Outline each uninfected red blood cell.
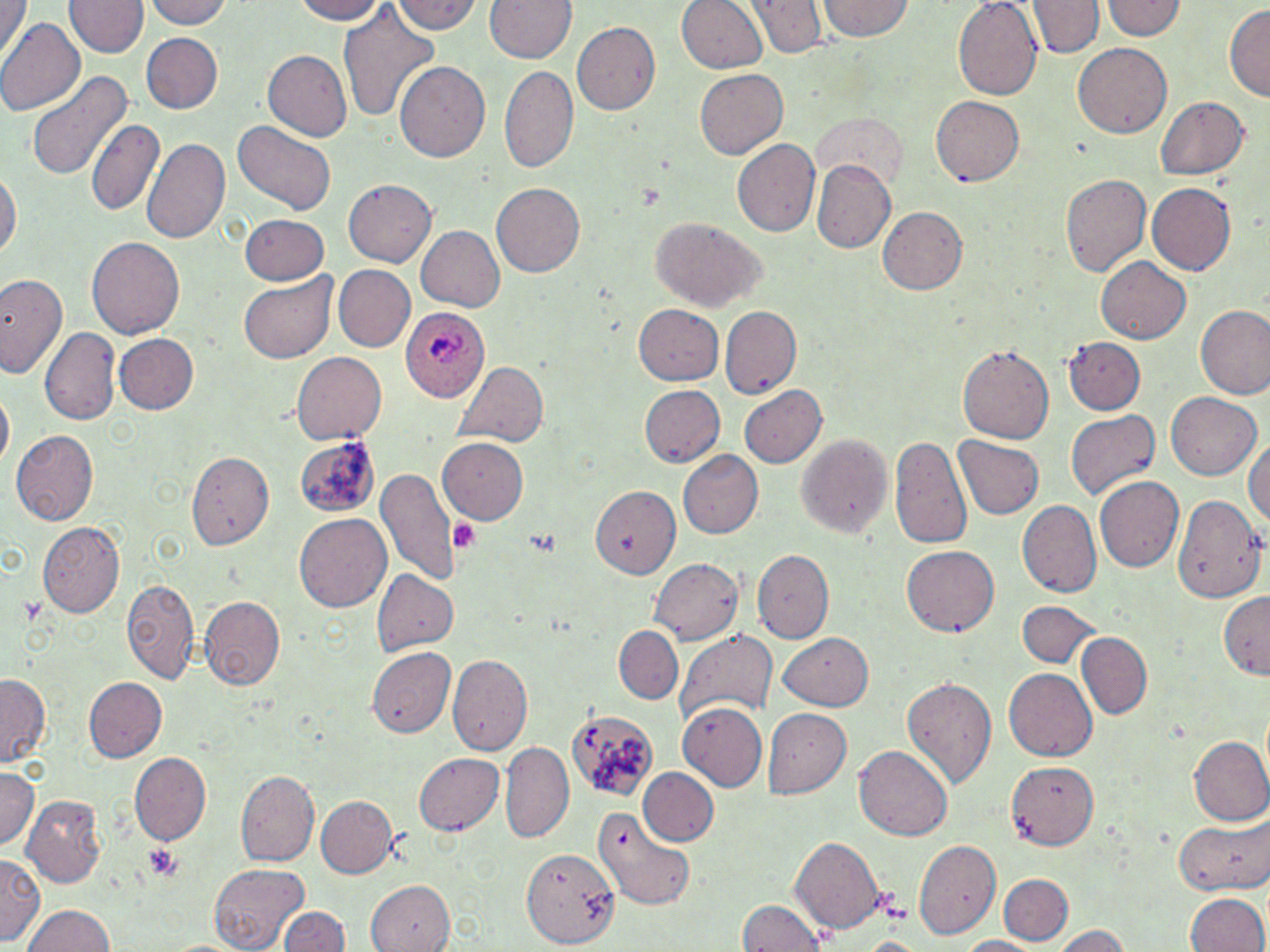
Approximate bounding boxes as (x1, y1, x2, y2) in pixels.
Uninfected red blood cells: (0, 0, 26, 61), (67, 0, 145, 58), (139, 0, 235, 28), (289, 0, 393, 24), (393, 0, 479, 37), (485, 0, 574, 64), (679, 0, 766, 74), (747, 0, 826, 58), (817, 0, 914, 42), (952, 0, 1042, 101), (1101, 0, 1184, 41), (1030, 2, 1100, 59), (1224, 5, 1269, 102), (339, 8, 440, 122), (0, 17, 85, 120), (572, 23, 660, 115), (139, 33, 224, 114), (1075, 43, 1169, 136), (263, 51, 352, 142), (395, 60, 490, 162), (501, 65, 577, 172), (694, 69, 787, 158), (26, 71, 131, 181), (930, 92, 1024, 184), (1154, 95, 1248, 181), (87, 118, 165, 218), (232, 123, 337, 215), (141, 139, 230, 245), (734, 140, 820, 237), (812, 159, 895, 253), (0, 166, 19, 269), (1059, 170, 1150, 275), (342, 179, 434, 267), (492, 183, 588, 277), (1147, 183, 1236, 276), (877, 206, 968, 294), (237, 215, 327, 284), (648, 218, 765, 313), (416, 227, 504, 310), (88, 237, 184, 337), (1096, 256, 1192, 343), (332, 265, 415, 354), (237, 272, 337, 364), (0, 275, 66, 377), (633, 305, 726, 387), (718, 305, 801, 400), (1195, 306, 1269, 399), (42, 326, 121, 427), (111, 332, 198, 415), (1061, 337, 1145, 416), (958, 344, 1054, 444), (292, 351, 386, 442), (453, 361, 547, 449), (738, 384, 828, 469), (639, 386, 725, 467), (1166, 393, 1261, 481), (1065, 409, 1159, 503), (12, 430, 98, 524), (891, 432, 973, 551), (798, 433, 893, 539), (292, 436, 380, 520), (954, 437, 1043, 520), (1245, 437, 1270, 536), (439, 440, 528, 524), (676, 450, 764, 540), (186, 452, 273, 552), (378, 468, 461, 586), (1095, 478, 1183, 572), (592, 485, 683, 577), (1172, 493, 1267, 602), (1017, 500, 1100, 599), (295, 515, 392, 612), (39, 523, 126, 617), (900, 546, 1000, 638), (753, 549, 833, 644), (649, 559, 744, 643), (374, 570, 460, 656), (121, 577, 199, 687), (1220, 590, 1270, 677), (200, 597, 285, 691), (1016, 602, 1098, 667), (614, 625, 683, 705), (674, 628, 777, 723), (778, 631, 876, 711), (1078, 632, 1152, 719), (367, 646, 454, 737), (448, 654, 533, 756), (1005, 670, 1096, 760), (0, 676, 51, 764), (84, 677, 167, 763), (902, 677, 997, 790), (677, 704, 767, 792), (564, 708, 659, 802), (764, 708, 852, 798), (1190, 737, 1270, 824), (500, 742, 574, 842), (854, 747, 954, 841), (130, 752, 211, 844), (415, 754, 505, 836), (1007, 763, 1099, 846), (636, 768, 718, 847), (0, 769, 40, 848), (236, 769, 318, 866), (315, 796, 396, 879), (23, 797, 106, 887), (593, 807, 697, 910), (1174, 815, 1269, 893), (791, 837, 882, 934), (914, 839, 1001, 940), (524, 845, 617, 948), (1, 854, 41, 944), (207, 863, 310, 950), (1001, 874, 1074, 944), (365, 880, 457, 952), (1184, 891, 1268, 952), (738, 900, 828, 952), (22, 905, 120, 952), (277, 905, 349, 952), (1049, 925, 1133, 952), (856, 936, 929, 952), (956, 936, 1042, 952), (154, 937, 256, 952).

Plasmodium ovale-infected red blood cell locations: (401, 304, 490, 401). Platelet locations: (449, 516, 481, 558), (142, 843, 184, 881). Slide-level diagnosis: Plasmodium ovale. May-Grünwald-Giemsa stain. Captured at 1000x magnification. Thin blood smear. Optical microscopy. Image is 1270×952 pixels. Single field of view.